Report the malaria status of this cell.
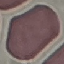
Uninfected.

Thin blood smear. Automatically extracted cell patch, resized to 64 × 64 pixels. Giemsa stain. Photographed with a smartphone camera at the microscope eyepiece.